Evaluate for Plasmodium parasites.
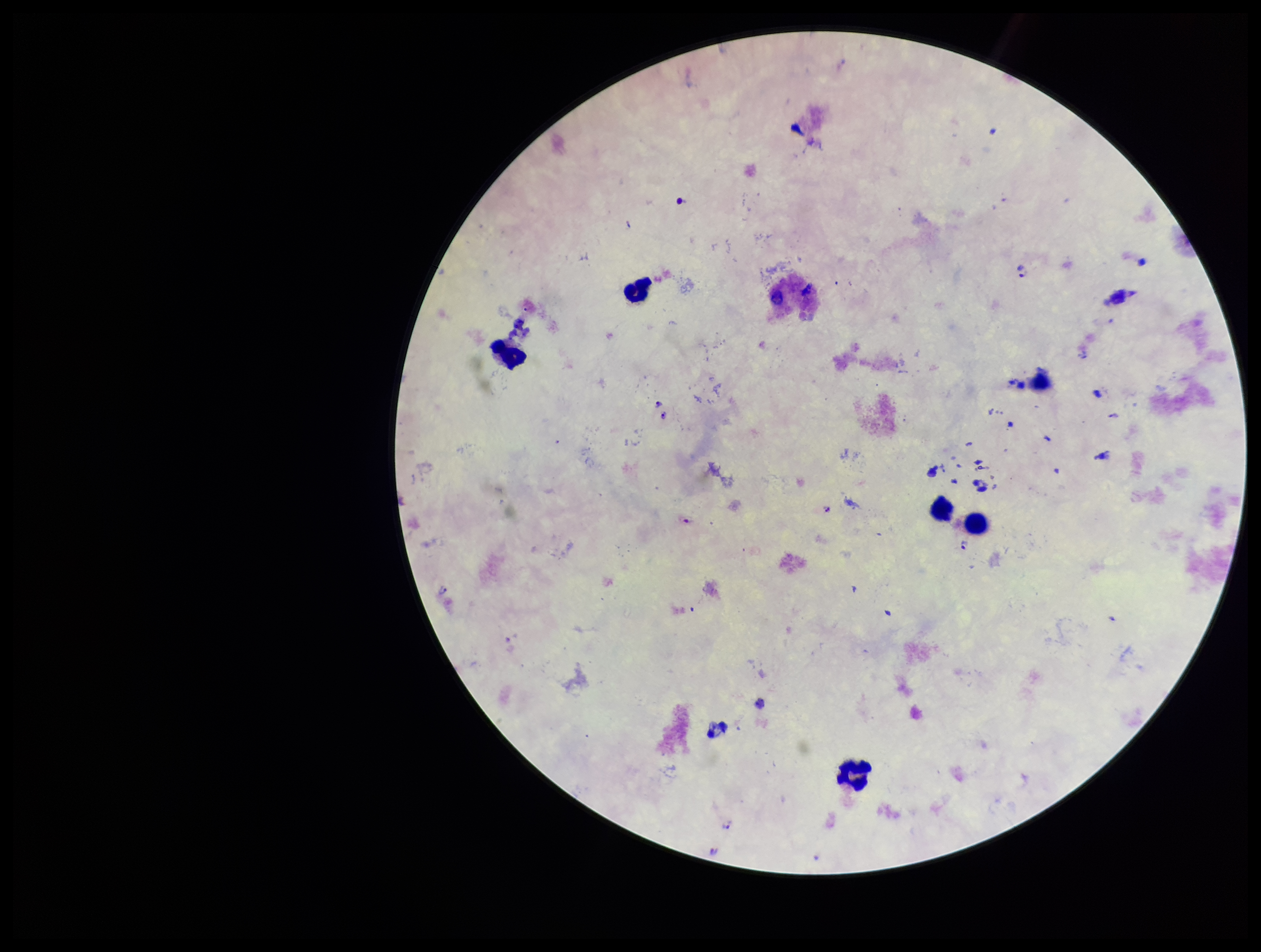

Identified.

Photographed through the microscope eyepiece with a smartphone camera. Leukocyte count: 7. Patient malaria status: infected. Giemsa stain. Image is 1261×952 pixels. Preparation: thick blood smear. Species reported for this patient: Plasmodium falciparum. Single field of view. Parasite count: 7.